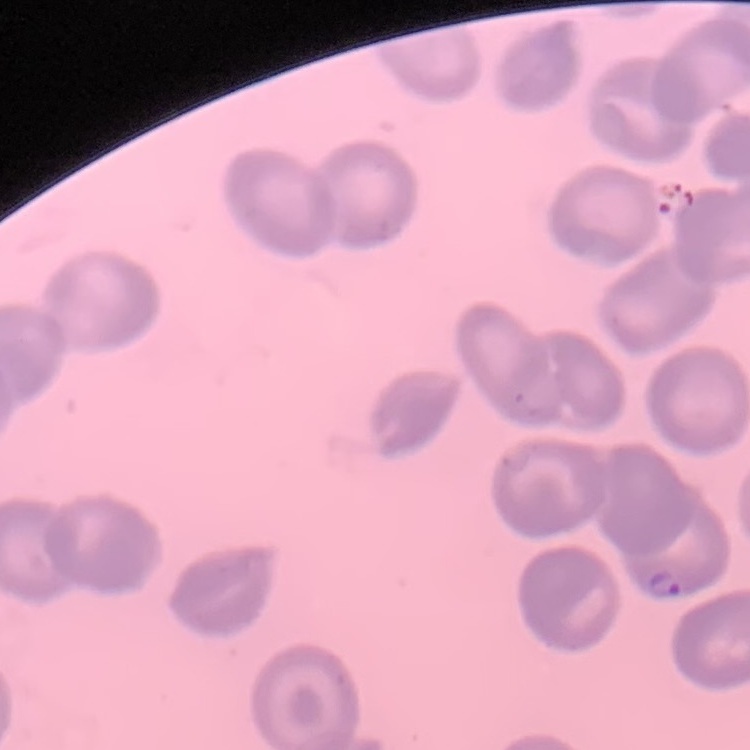
The red blood cells show no rouleaux formation. Stained with either Field's or Giemsa. Thin blood smear. Square crop of a larger photomicrograph.